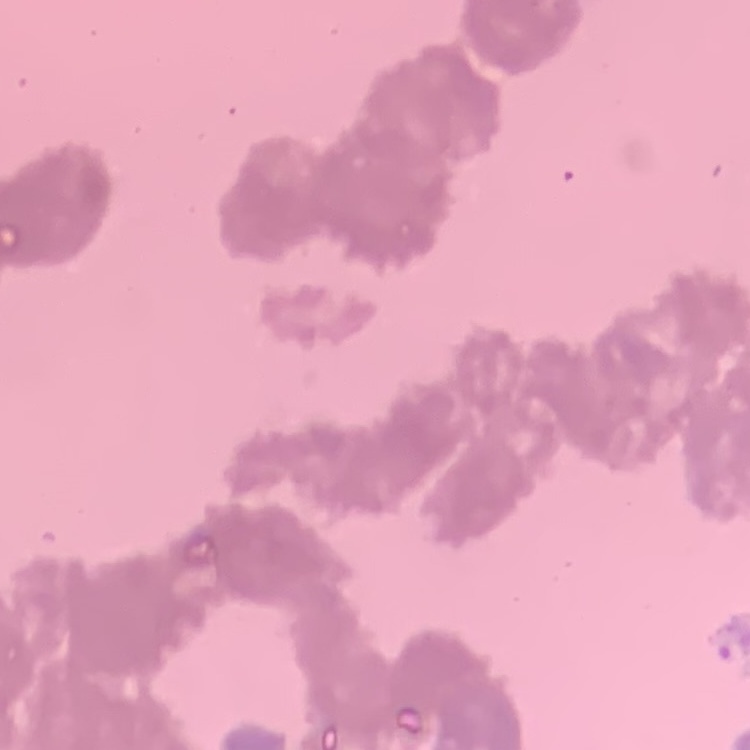 The erythrocytes show rouleaux formation. Thin peripheral smear. Field's or Giemsa stain. One tile cut from a larger photomicrograph.